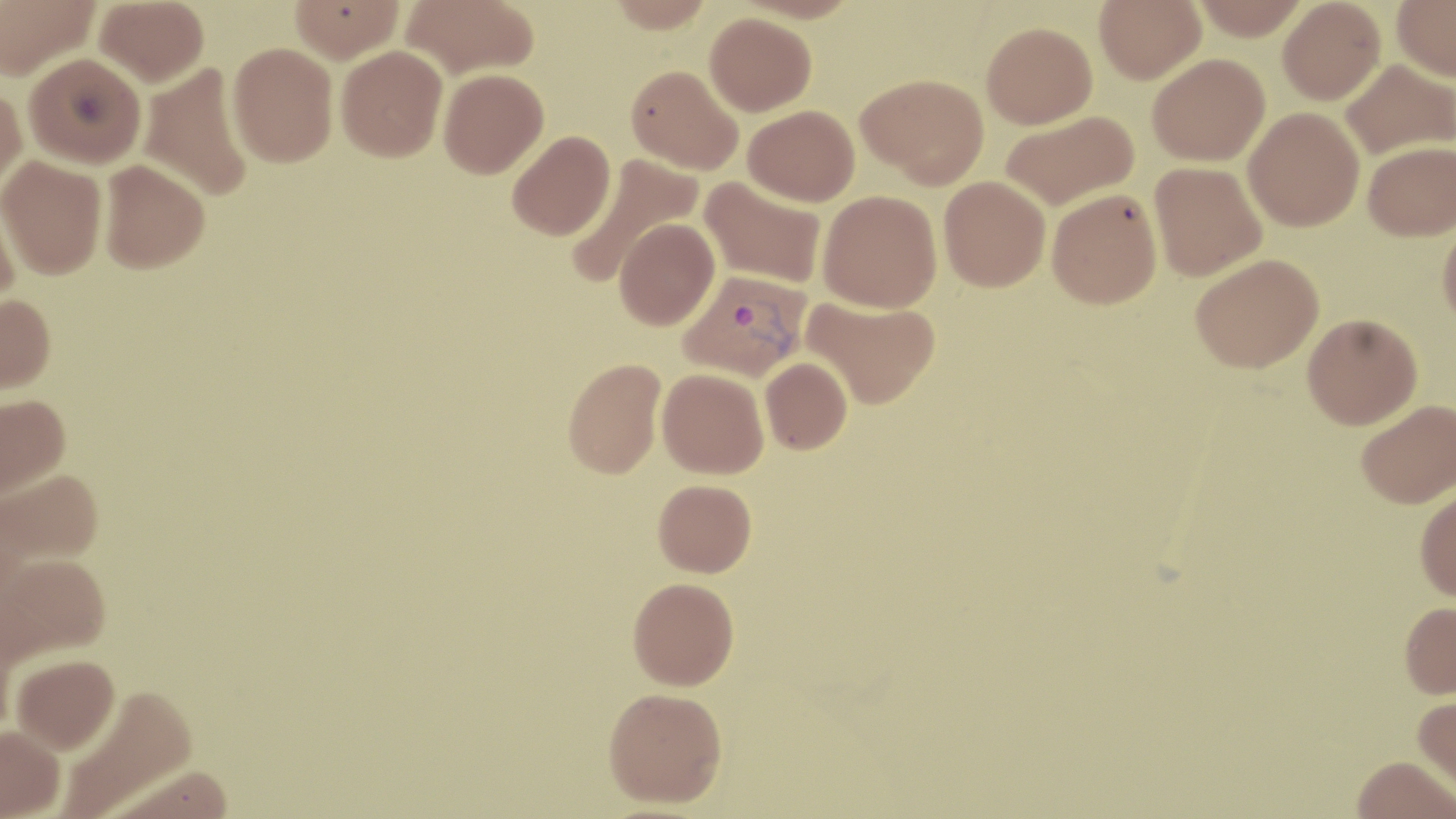

{
  "slide_level_diagnosis": "Plasmodium vivax",
  "field_of_view": "one of a larger specimen",
  "preparation": "thin blood film",
  "uninfected_red_blood_cell_locations": "approximate bounding boxes as named x1/y1/x2/y2 corners in pixels: (x1=0, y1=0, x2=101, y2=81), (x1=94, y1=0, x2=209, y2=87), (x1=402, y1=0, x2=539, y2=78), (x1=605, y1=0, x2=717, y2=33), (x1=1094, y1=0, x2=1205, y2=83), (x1=1191, y1=0, x2=1311, y2=40), (x1=1278, y1=0, x2=1386, y2=104), (x1=1391, y1=0, x2=1456, y2=81), (x1=289, y1=1, x2=404, y2=63), (x1=705, y1=12, x2=817, y2=115), (x1=982, y1=21, x2=1097, y2=128), (x1=228, y1=42, x2=338, y2=167), (x1=336, y1=45, x2=447, y2=161), (x1=24, y1=52, x2=146, y2=168), (x1=1147, y1=53, x2=1270, y2=166), (x1=1340, y1=59, x2=1455, y2=160), (x1=137, y1=63, x2=254, y2=202), (x1=626, y1=65, x2=743, y2=175), (x1=439, y1=68, x2=548, y2=178), (x1=858, y1=73, x2=989, y2=188), (x1=0, y1=83, x2=27, y2=194), (x1=743, y1=104, x2=859, y2=206), (x1=1243, y1=107, x2=1365, y2=231), (x1=1000, y1=111, x2=1139, y2=211), (x1=507, y1=130, x2=615, y2=240), (x1=1363, y1=141, x2=1456, y2=241), (x1=564, y1=153, x2=703, y2=289), (x1=0, y1=155, x2=107, y2=279), (x1=98, y1=159, x2=210, y2=273), (x1=1148, y1=161, x2=1266, y2=281), (x1=939, y1=175, x2=1050, y2=291), (x1=699, y1=176, x2=827, y2=290), (x1=0, y1=186, x2=21, y2=311), (x1=1047, y1=188, x2=1162, y2=309), (x1=818, y1=190, x2=942, y2=312), (x1=614, y1=217, x2=720, y2=330), (x1=1438, y1=217, x2=1456, y2=329), (x1=1190, y1=253, x2=1323, y2=373), (x1=0, y1=294, x2=56, y2=394), (x1=802, y1=295, x2=941, y2=409), (x1=1302, y1=314, x2=1422, y2=429), (x1=760, y1=357, x2=852, y2=454), (x1=562, y1=358, x2=665, y2=479), (x1=657, y1=368, x2=769, y2=479), (x1=0, y1=393, x2=71, y2=500), (x1=1356, y1=399, x2=1456, y2=509), (x1=0, y1=469, x2=104, y2=569), (x1=653, y1=479, x2=757, y2=577), (x1=1415, y1=486, x2=1456, y2=602), (x1=1, y1=554, x2=113, y2=667), (x1=628, y1=577, x2=739, y2=690), (x1=1399, y1=600, x2=1456, y2=698), (x1=11, y1=654, x2=121, y2=756), (x1=57, y1=684, x2=199, y2=817), (x1=604, y1=686, x2=727, y2=807), (x1=1413, y1=694, x2=1456, y2=797), (x1=1382, y1=712, x2=1456, y2=794), (x1=0, y1=725, x2=65, y2=819), (x1=1351, y1=756, x2=1456, y2=819)",
  "plasmodium_vivax_infected_red_blood_cell_locations": "approximate bounding boxes as named x1/y1/x2/y2 corners in pixels: (x1=679, y1=269, x2=810, y2=382)",
  "image_size": "1456×819 pixels",
  "modality": "light microscopy",
  "stain": "May-Grünwald-Giemsa",
  "magnification": "1000x"
}